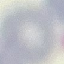
Summary:
  - Result: negative for malaria parasites
  - Image type: cell patch, automatically extracted from a larger field of view and resized to 64 × 64 pixels
  - Capture: smartphone through the microscope eyepiece
  - Preparation: thin blood smear
  - Stain: Giemsa